Identify the cell.
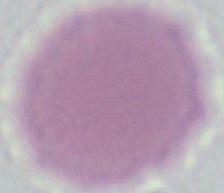
This is an erythrocyte.

{
  "modality": "photomicrograph",
  "magnification": "1000x"
}